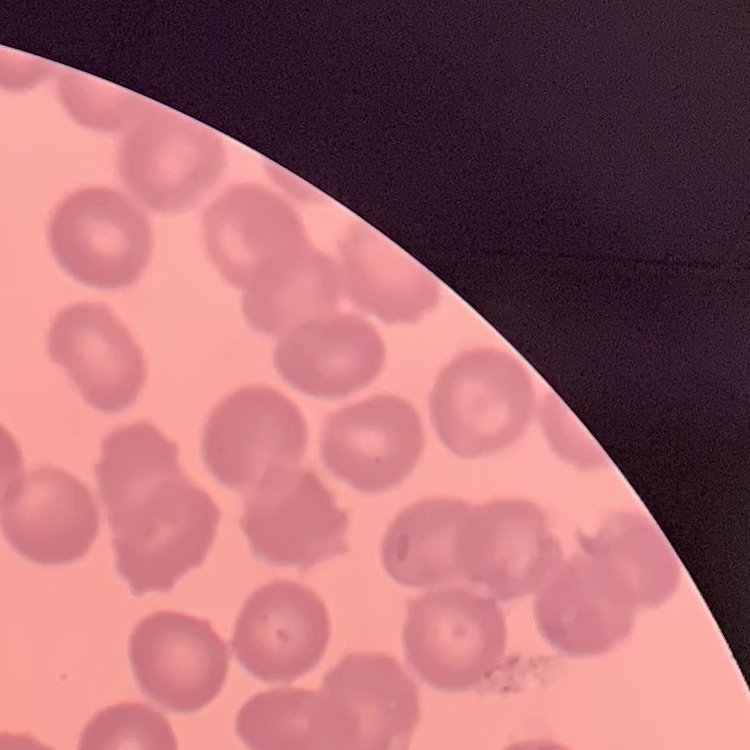
{
  "red_blood_cell_morphology": "no rouleaux formation",
  "stain": "Field's or Giemsa",
  "preparation": "thin blood film",
  "image_type": "one tile cut from a larger photomicrograph"
}